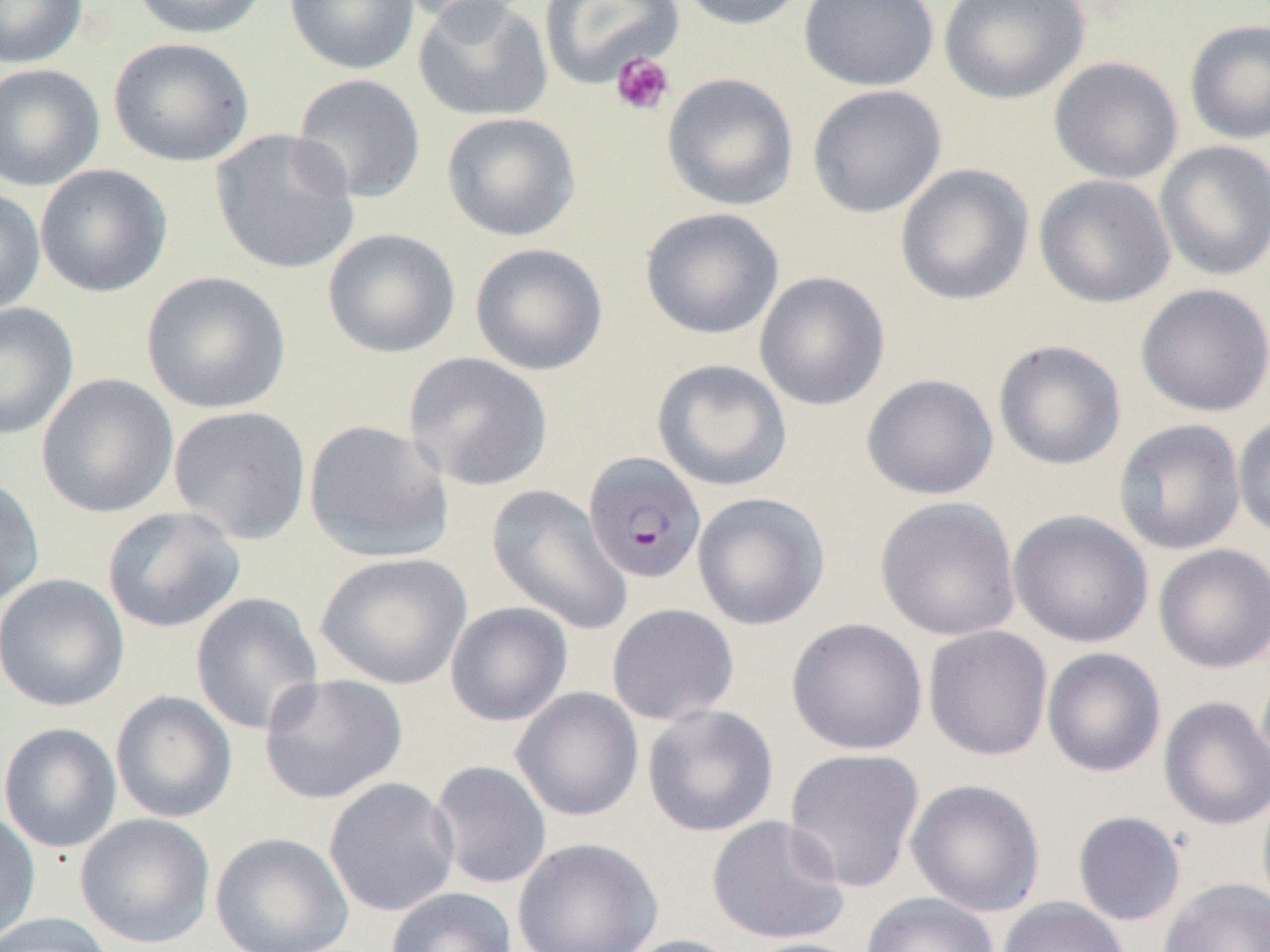

Summary:
  - Coordinate format: approximate bounding boxes as [x1, y1, x2, y2] in pixels
  - Platelet locations: [610, 51, 675, 116]
  - Uninfected red blood cell locations: [0, 0, 88, 68], [130, 0, 268, 39], [285, 0, 420, 75], [394, 0, 538, 29], [413, 0, 554, 123], [539, 0, 683, 88], [675, 0, 812, 31], [799, 0, 939, 91], [939, 0, 1089, 104], [1184, 18, 1270, 145], [108, 37, 255, 167], [1048, 57, 1183, 184], [0, 63, 105, 191], [662, 72, 799, 211], [291, 73, 427, 204], [807, 84, 946, 218], [441, 111, 581, 242], [209, 128, 360, 275], [1154, 140, 1270, 282], [895, 163, 1033, 306], [35, 164, 172, 297], [1034, 173, 1175, 309], [0, 187, 46, 317], [639, 207, 784, 340], [323, 228, 460, 358], [469, 242, 608, 376], [141, 271, 291, 415], [754, 271, 890, 411], [1135, 283, 1270, 418], [0, 302, 79, 440], [993, 339, 1126, 470], [404, 352, 553, 492], [651, 358, 792, 491], [860, 373, 999, 500], [36, 374, 179, 519], [168, 405, 312, 545], [1232, 412, 1270, 541], [1113, 418, 1246, 555], [303, 419, 454, 562], [0, 475, 45, 611], [487, 484, 633, 635], [692, 492, 830, 630], [875, 496, 1022, 641], [101, 506, 245, 633], [1008, 509, 1154, 648], [1153, 543, 1270, 674], [315, 551, 472, 690], [0, 573, 130, 713], [190, 592, 324, 735], [445, 601, 573, 727], [606, 603, 740, 726], [786, 617, 928, 755], [923, 625, 1053, 761], [1042, 647, 1166, 778], [258, 672, 408, 805], [511, 687, 644, 822], [110, 690, 237, 823], [1158, 696, 1270, 830], [642, 703, 778, 837], [0, 722, 122, 854], [783, 747, 925, 892], [428, 759, 553, 889], [324, 777, 460, 917], [905, 778, 1046, 917], [1256, 783, 1270, 917], [0, 807, 40, 946], [1072, 811, 1186, 926], [75, 813, 216, 949], [706, 814, 850, 945], [209, 832, 355, 952], [512, 836, 663, 952], [1158, 877, 1270, 952], [385, 887, 517, 952], [861, 892, 999, 952], [997, 897, 1130, 952], [0, 912, 116, 952], [615, 934, 744, 952], [737, 937, 866, 952]
  - Plasmodium falciparum-infected red blood cell locations: [582, 451, 707, 585]
  - Slide-level diagnosis: Plasmodium falciparum
  - Image size: 1270×952 pixels
  - Modality: light microscopy
  - Field of view: single
  - Magnification: 1000x
  - Preparation: thin blood film